State the preparation type.
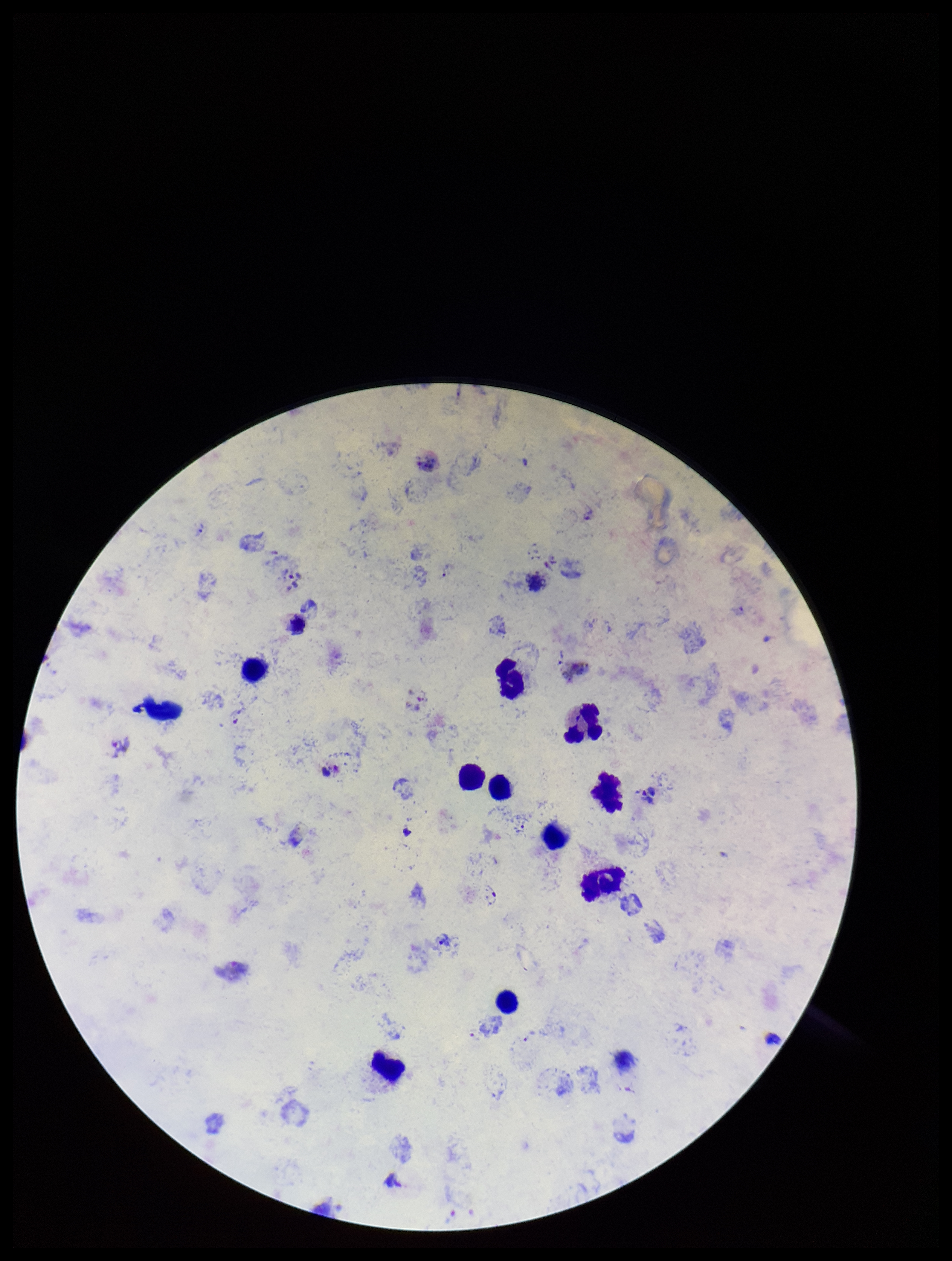

A thick smear.

Summary:
  - Patient malaria status: positive
  - Parasite count: 4
  - Image size: 952×1261 pixels
  - Field of view: one from this slide
  - Stain: Giemsa
  - Leukocyte count: 11
  - Species reported for this patient: Plasmodium vivax
  - Capture: smartphone photograph through the microscope eyepiece
  - Plasmodium parasites: seen